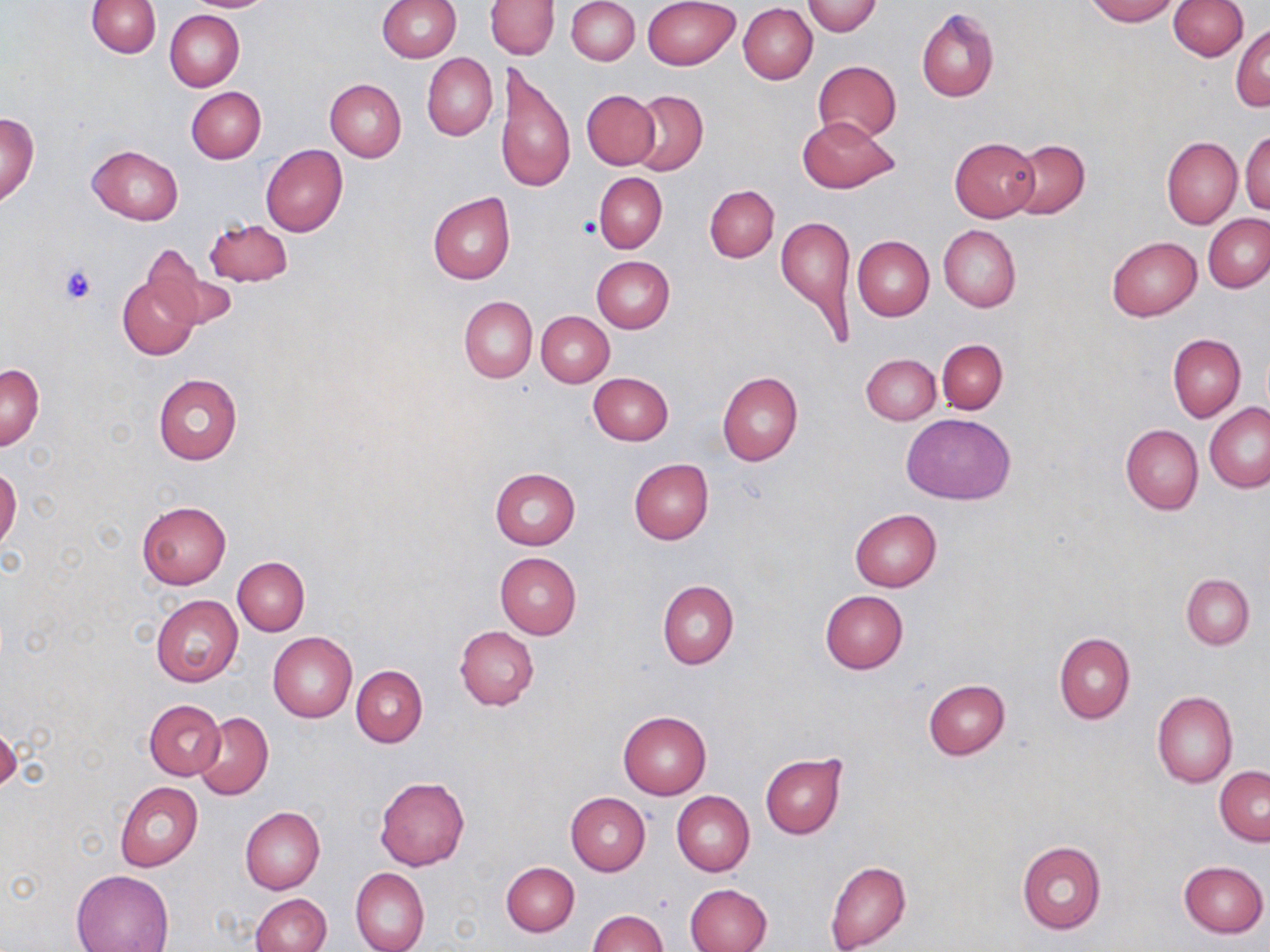

Summary:
  - Coordinate format: approximate bounding boxes as (x1, y1, x2, y2) in pixels
  - Uninfected red blood cell locations: (184, 0, 275, 12), (377, 0, 461, 62), (567, 0, 640, 66), (1085, 0, 1178, 25), (1168, 0, 1248, 60), (87, 1, 160, 57), (487, 1, 557, 59), (643, 1, 741, 68), (801, 1, 883, 36), (739, 4, 817, 84), (916, 8, 999, 102), (164, 10, 244, 92), (1231, 24, 1269, 112), (422, 53, 497, 140), (813, 60, 901, 143), (495, 62, 575, 195), (325, 79, 406, 161), (186, 86, 265, 162), (582, 89, 660, 169), (629, 89, 707, 175), (0, 112, 41, 205), (797, 115, 899, 194), (1241, 129, 1270, 215), (950, 137, 1039, 221), (1162, 137, 1241, 228), (1007, 139, 1089, 219), (88, 145, 184, 225), (261, 145, 348, 236), (594, 172, 667, 252), (704, 185, 778, 262), (428, 192, 515, 285), (775, 213, 858, 343), (1204, 214, 1270, 291), (205, 219, 292, 287), (939, 224, 1021, 312), (852, 235, 934, 321), (1107, 236, 1201, 321), (143, 252, 237, 329), (591, 256, 674, 334), (118, 267, 202, 358), (459, 296, 537, 383), (537, 311, 614, 386), (1167, 333, 1245, 422), (937, 339, 1008, 413), (861, 353, 941, 424), (1, 363, 44, 450), (717, 371, 802, 465), (153, 372, 242, 465), (589, 373, 673, 445), (1205, 404, 1270, 493), (902, 414, 1016, 503), (1121, 425, 1204, 514), (628, 458, 713, 545), (0, 467, 22, 552), (489, 468, 581, 549), (137, 501, 232, 588), (849, 508, 942, 591), (495, 553, 582, 638), (233, 558, 309, 635), (1181, 574, 1254, 649), (657, 581, 738, 669), (820, 590, 908, 673), (150, 593, 243, 687), (455, 625, 539, 710), (268, 632, 358, 723), (1054, 632, 1135, 724), (351, 665, 428, 746), (923, 680, 1010, 759), (1152, 691, 1237, 788), (145, 699, 225, 779), (193, 712, 273, 800), (618, 712, 712, 799), (760, 753, 847, 838), (1215, 766, 1270, 845), (375, 777, 471, 871), (116, 782, 203, 870), (672, 791, 754, 876), (565, 792, 650, 876), (240, 807, 325, 894), (1017, 841, 1106, 933), (824, 859, 910, 952), (1178, 860, 1267, 938), (501, 862, 579, 936), (351, 867, 430, 952), (70, 869, 174, 952), (684, 884, 771, 952), (251, 893, 330, 952), (589, 911, 669, 952)
  - Platelet locations: (581, 215, 602, 239), (60, 263, 95, 304)
  - Slide-level diagnosis: no evidence of blood parasites
  - Preparation: thin blood film
  - Field of view: one of a larger specimen
  - Image size: 1270×952 pixels
  - Magnification: 1000x
  - Modality: light microscopy
  - Stain: May-Grünwald-Giemsa